State which parasite is depicted.
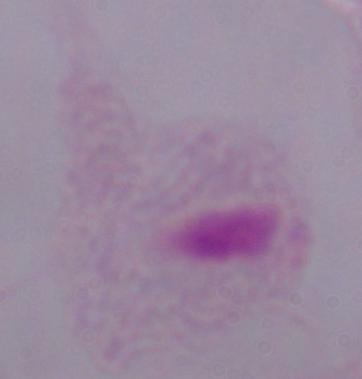
This is a trichomonad.

{
  "magnification": "1000x",
  "modality": "photomicrograph"
}